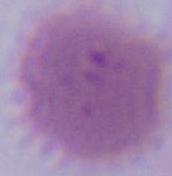

Summary:
  - Identification: red blood cell
  - Modality: micrograph
  - Magnification: 1000x